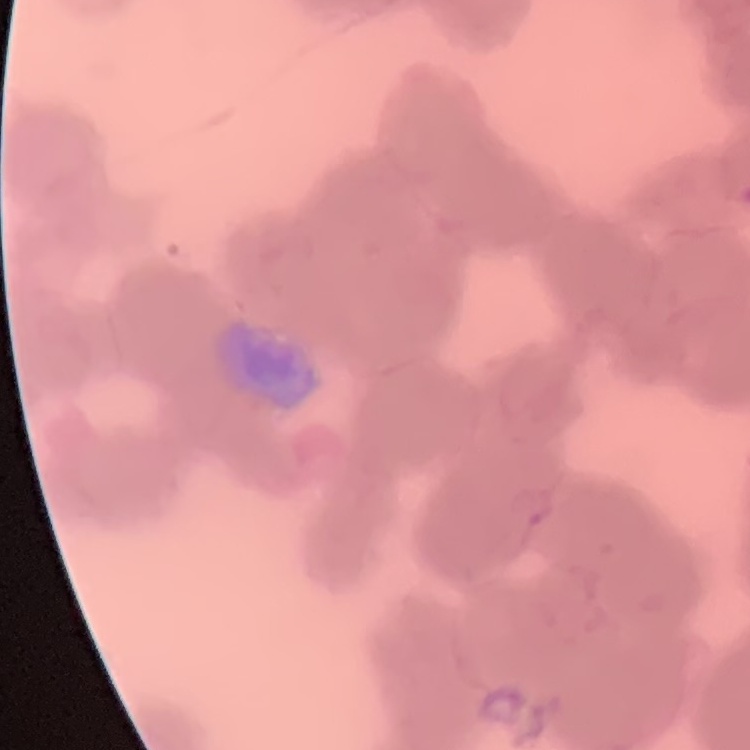

Summary:
  - Erythrocyte morphology: rouleaux formation
  - Preparation: thin peripheral smear
  - Image type: one tile cut from a larger photomicrograph
  - Stain: Field's or Giemsa